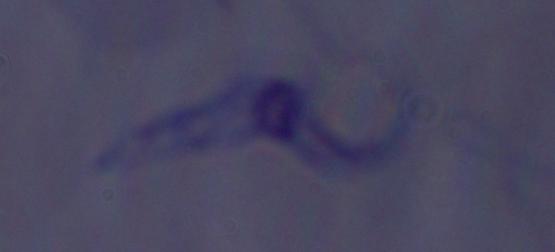
A trypanosome is seen. 1000x magnification. Micrograph.